Report the malaria status of this cell.
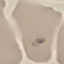
Parasitized.

{
  "stain": "Giemsa",
  "image_type": "automatically extracted cell patch, resized to 64 × 64 pixels",
  "preparation": "thin blood film",
  "capture": "smartphone camera at the microscope eyepiece"
}